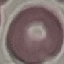
malaria_status: uninfected
stain: Giemsa
capture: smartphone camera at the microscope eyepiece
image_type: automatically extracted cell patch, resized to 64 × 64 pixels
preparation: thin blood smear